Give the position of every leukocyte visible.
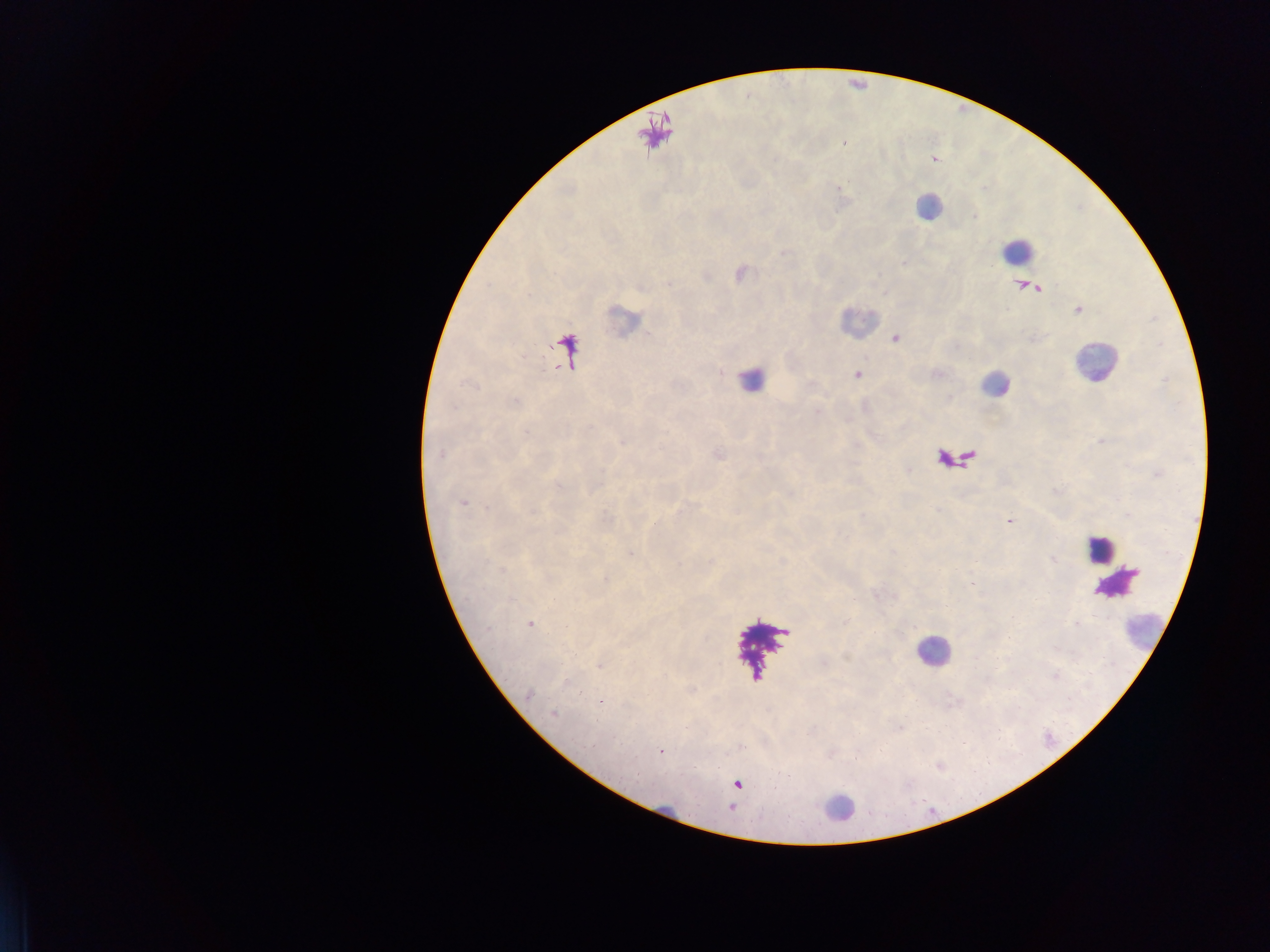

Approximate centers as {x, y} in pixels.
Leukocytes: {928, 206}, {1017, 249}, {1094, 361}, {751, 378}, {994, 384}, {1099, 548}, {1114, 584}, {1143, 633}, {932, 650}, {836, 809}, {670, 815}.

image size = 1270×952 pixels
country = Ghana
capture = mobile-phone photograph through a microscope
malaria parasite locations = approximate centers as {x, y} in pixels: {857, 374}, {440, 454}, {462, 503}, {1010, 521}, {630, 554}, {530, 624}, {528, 693}, {601, 701}, {553, 713}, {660, 752}
preparation = thick blood film
field of view = single